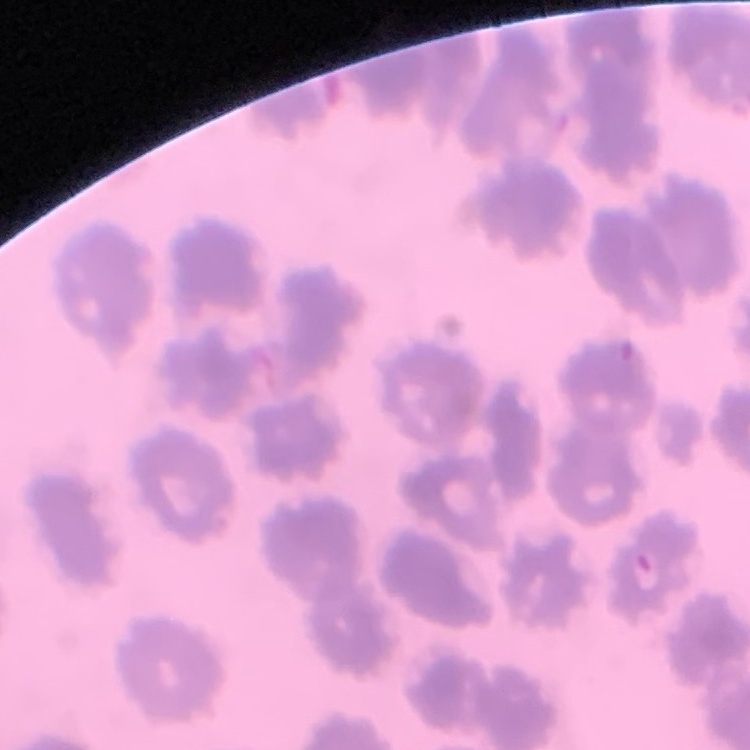 The erythrocytes exhibit no rouleaux formation. Field's or Giemsa stain. One tile cut from a larger photomicrograph. Thin blood smear.